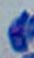

Photomicrograph. Captured at 1000x magnification. Toxoplasma gondii is seen.